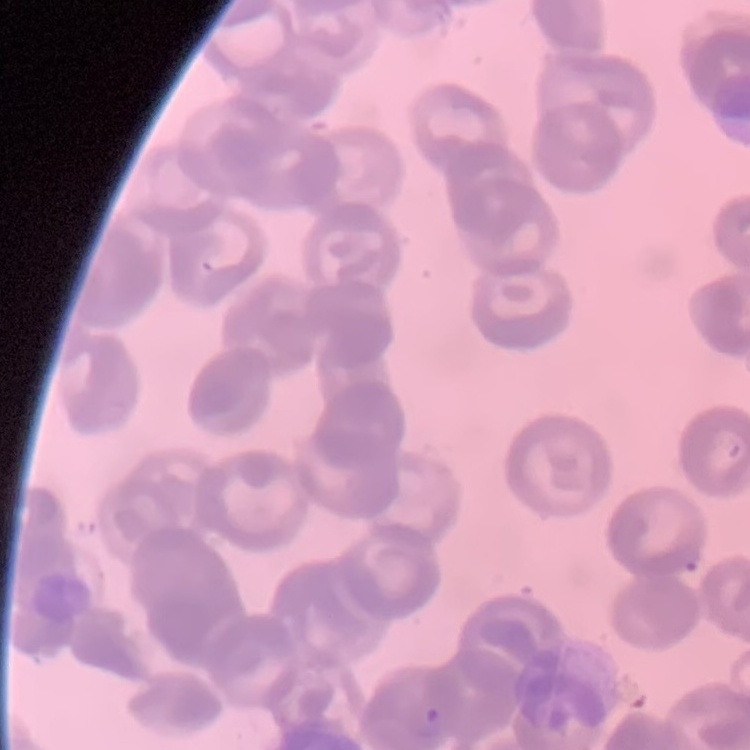
erythrocyte morphology = rouleaux formation
image type = square crop of a larger photomicrograph
preparation = thin blood film
stain = Field's or Giemsa